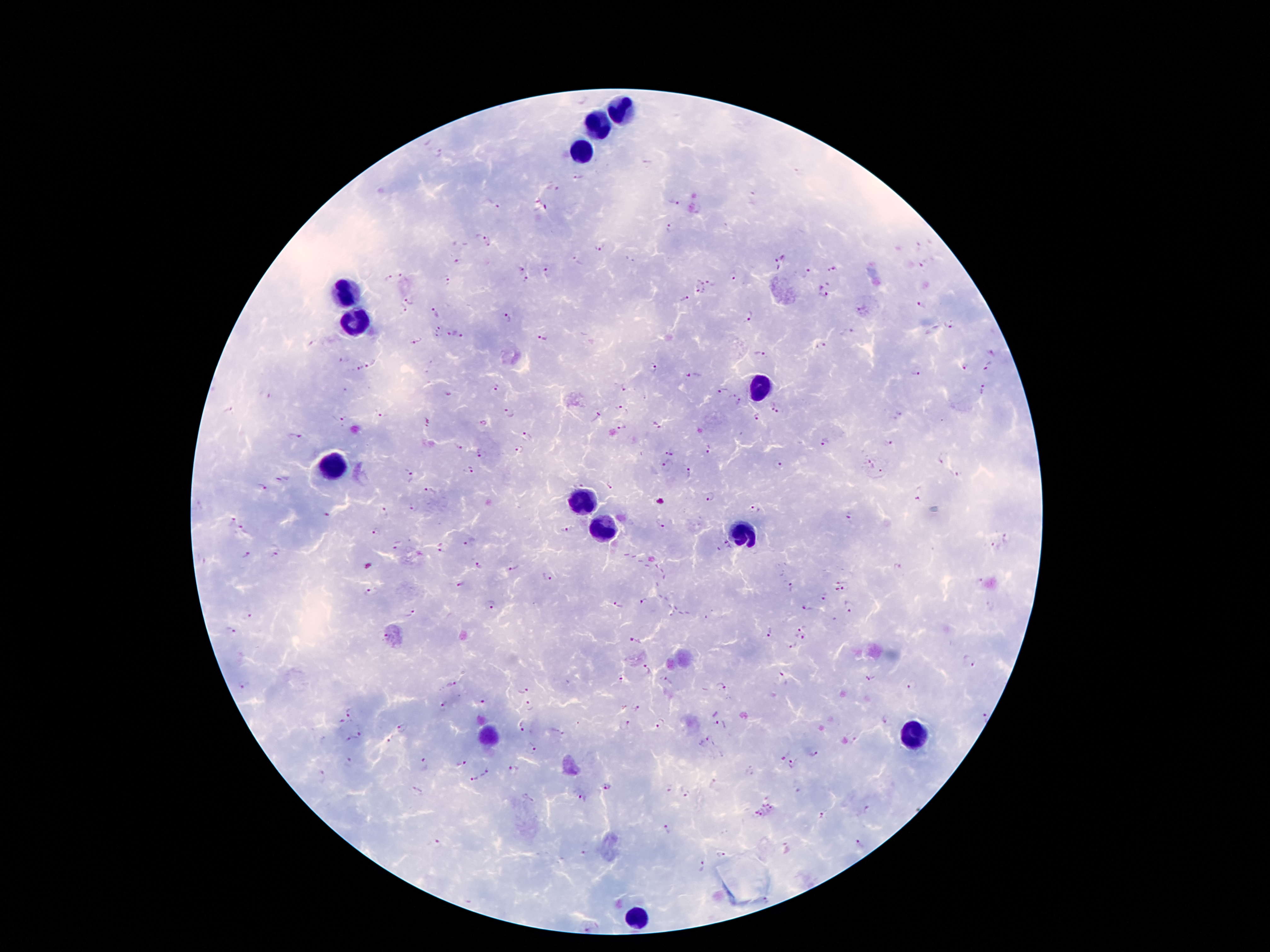

Patient malaria status: infected with Plasmodium falciparum. Single field of view. 100x magnification. Photographed through the microscope eyepiece with a smartphone camera. Thick blood smear. Image is 1270×952 pixels. Giemsa-stained preparation.